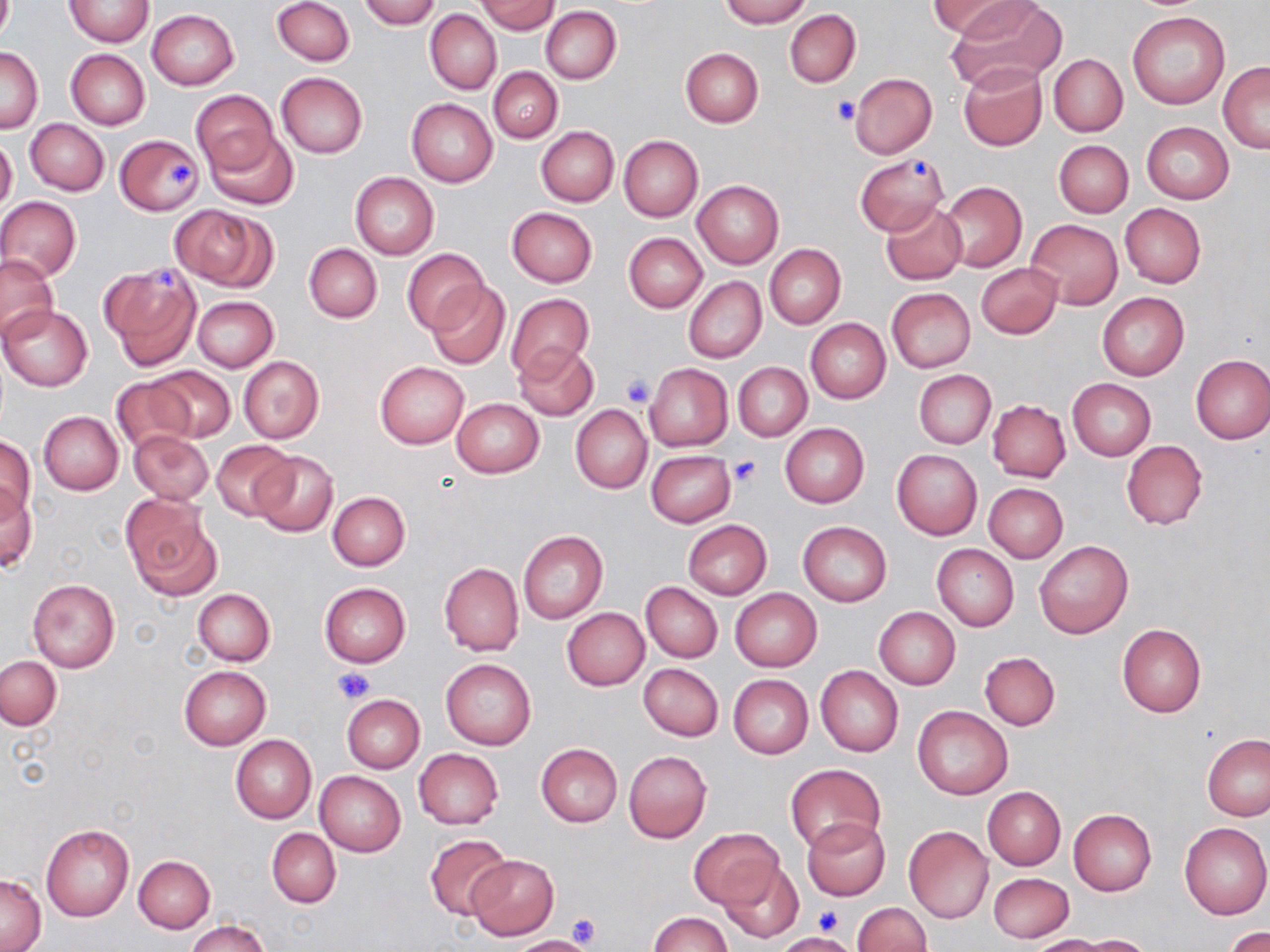
{
  "slide_level_diagnosis": "no evidence of blood parasites",
  "magnification": "1000x",
  "modality": "optical microscopy",
  "stain": "May-Grünwald-Giemsa",
  "platelet_locations": "approximate bounding boxes as (x1,y1)-(x2,y2) corner pairs in pixels: (831,96)-(858,125), (910,159)-(933,179), (166,160)-(197,187), (155,266)-(180,292), (622,376)-(654,408), (727,456)-(761,488), (332,665)-(374,704), (816,903)-(843,935), (566,913)-(600,949)",
  "preparation": "thin blood film",
  "uninfected_red_blood_cell_locations": "approximate bounding boxes as (x1,y1)-(x2,y2) corner pairs in pixels: (64,0)-(153,47), (272,0)-(354,65), (359,0)-(440,29), (720,0)-(810,27), (928,0)-(1032,38), (949,0)-(1065,86), (475,1)-(560,34), (541,6)-(622,84), (426,9)-(502,95), (784,9)-(860,88), (147,10)-(238,90), (1127,11)-(1230,110), (1,45)-(43,133), (679,47)-(764,127), (65,50)-(149,129), (1049,54)-(1127,136), (1218,61)-(1269,152), (958,63)-(1047,151), (488,66)-(562,143), (276,72)-(368,158), (849,72)-(936,158), (192,89)-(278,175), (406,99)-(497,188), (27,119)-(108,195), (1142,121)-(1233,204), (535,125)-(618,206), (204,127)-(298,210), (0,134)-(17,215), (114,134)-(202,216), (619,135)-(702,221), (1054,140)-(1133,218), (856,154)-(947,235), (349,173)-(438,259), (692,180)-(784,269), (939,180)-(1026,272), (0,196)-(81,280), (881,201)-(968,284), (1120,203)-(1206,288), (168,204)-(273,289), (506,208)-(597,287), (1026,218)-(1123,308), (624,233)-(707,312), (303,244)-(382,323), (765,244)-(845,328), (403,248)-(491,335), (0,255)-(59,341), (976,262)-(1063,339), (100,263)-(203,370), (684,276)-(766,364), (426,280)-(511,370), (886,288)-(975,373), (1097,292)-(1189,381), (506,293)-(594,381), (192,296)-(279,372), (1,305)-(92,390), (806,319)-(891,403), (512,342)-(598,420), (1190,354)-(1270,444), (239,357)-(323,443), (375,362)-(468,448), (733,362)-(811,442), (643,363)-(733,452), (145,366)-(236,442), (914,370)-(996,449), (109,376)-(195,455), (1069,378)-(1156,461), (450,397)-(545,479), (987,400)-(1070,481), (571,404)-(652,493), (39,411)-(124,495), (780,423)-(869,508), (128,430)-(213,505), (0,437)-(35,522), (1120,439)-(1208,531), (212,440)-(295,519), (892,449)-(982,540), (646,450)-(736,527), (251,451)-(338,537), (983,483)-(1068,563), (1,485)-(37,575), (326,491)-(410,571), (124,497)-(220,600), (683,521)-(772,599), (798,521)-(892,607), (517,529)-(608,624), (1034,541)-(1133,638), (931,544)-(1018,632), (438,561)-(523,656), (28,578)-(120,672), (641,582)-(722,663), (319,583)-(411,667), (192,588)-(274,666), (730,588)-(821,672), (562,607)-(650,690), (874,607)-(960,689), (1117,623)-(1206,719), (980,652)-(1060,730), (1,656)-(61,729), (441,658)-(536,750), (638,663)-(724,741), (815,665)-(903,757), (180,666)-(270,751), (728,674)-(813,759), (342,694)-(424,774), (912,705)-(1012,800), (231,734)-(316,823), (1202,734)-(1270,821), (536,743)-(622,827), (413,749)-(504,828), (623,750)-(712,842), (785,763)-(886,855), (314,771)-(406,856), (983,787)-(1066,870), (1068,810)-(1156,896), (801,817)-(889,900), (1180,822)-(1270,920), (41,824)-(134,922), (903,826)-(993,923), (266,828)-(341,907), (690,828)-(782,909), (424,833)-(512,921), (133,854)-(215,932), (466,855)-(559,940), (718,861)-(804,944), (988,872)-(1074,943), (0,874)-(46,951), (852,902)-(933,952), (648,912)-(733,952), (184,918)-(270,952), (1225,926)-(1270,952), (1076,934)-(1155,951), (512,935)-(598,952), (1027,935)-(1115,952)",
  "field_of_view": "one of a larger specimen",
  "image_size": "1270×952 pixels"
}